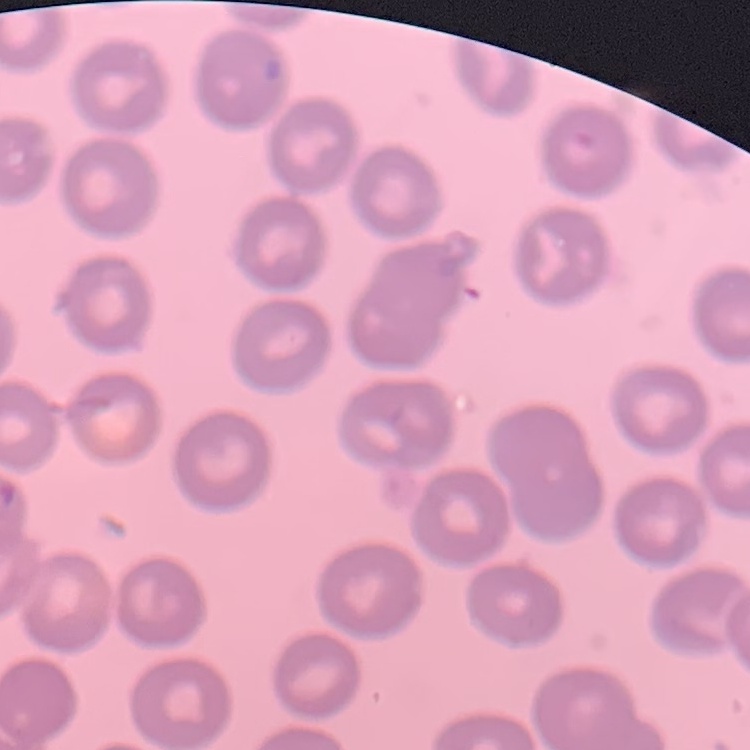

Summary:
  - Red blood cell morphology: no rouleaux formation
  - Preparation: thin blood film
  - Stain: Field's or Giemsa
  - Image type: square crop of a larger photomicrograph